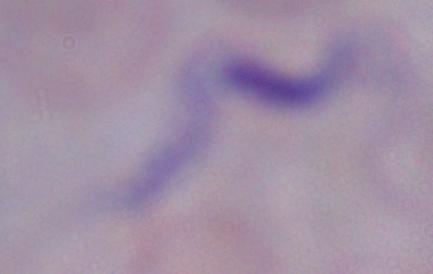

A trypanosome is seen. Photomicrograph. Captured at 1000x magnification.